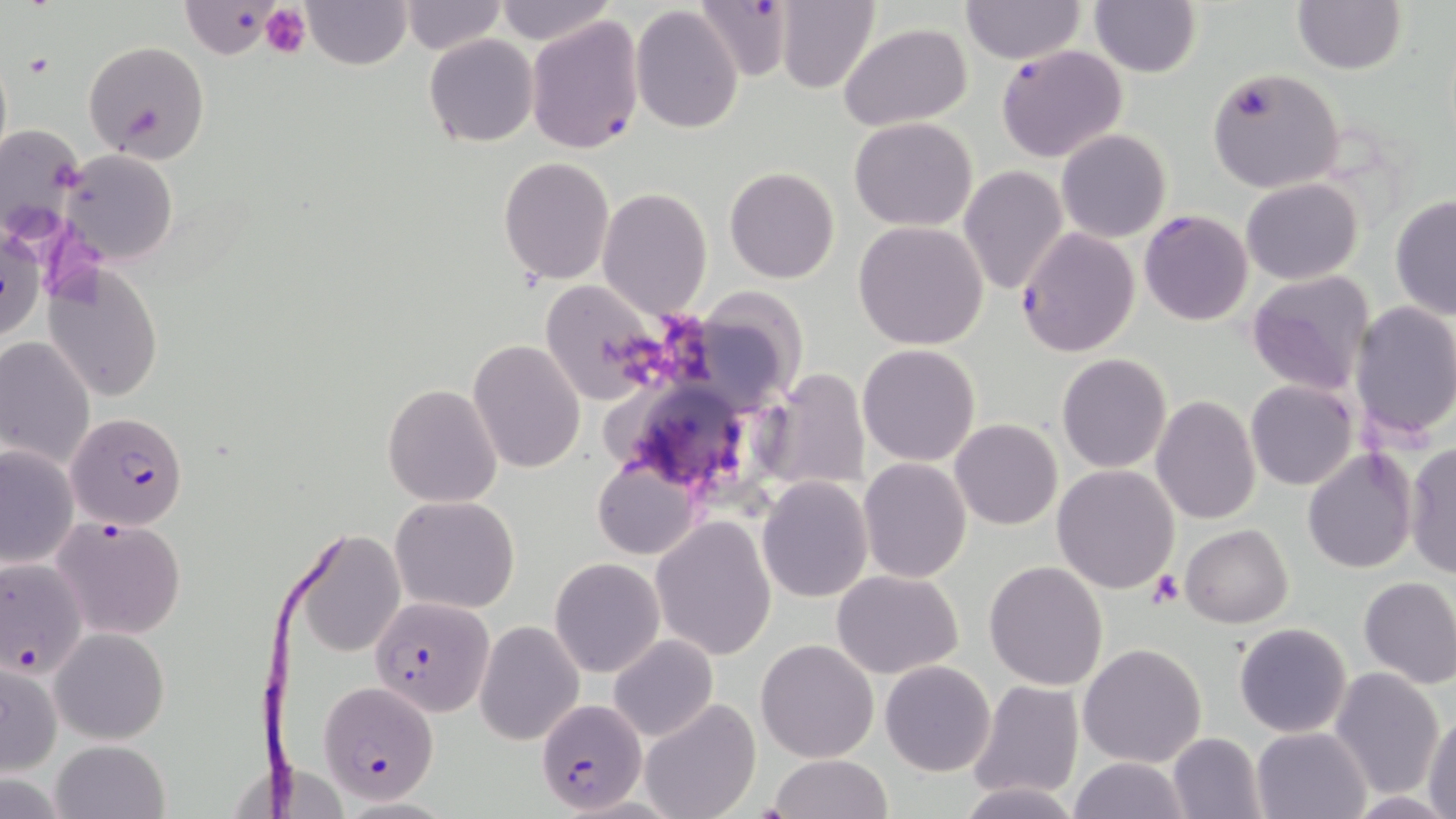
{
  "slide_level_diagnosis": "Plasmodium falciparum",
  "uninfected_red_blood_cell_locations": "approximate bounding boxes as (x1, y1, x2, y2) in pixels: (179, 0, 291, 60), (305, 0, 410, 70), (401, 0, 506, 55), (774, 0, 881, 94), (1088, 0, 1201, 77), (1292, 0, 1406, 74), (491, 1, 615, 47), (960, 1, 1087, 64), (631, 4, 743, 135), (838, 23, 970, 131), (424, 33, 537, 146), (83, 40, 210, 164), (1207, 68, 1346, 193), (848, 117, 977, 231), (1057, 130, 1171, 243), (58, 148, 179, 264), (499, 157, 614, 285), (958, 167, 1068, 295), (724, 168, 839, 283), (1242, 178, 1364, 285), (598, 187, 712, 320), (1389, 194, 1456, 320), (852, 222, 990, 351), (1, 225, 43, 346), (44, 265, 164, 403), (1247, 269, 1373, 397), (538, 281, 666, 404), (1349, 302, 1456, 441), (1, 336, 94, 472), (467, 340, 586, 475), (857, 343, 981, 466), (1057, 354, 1171, 473), (757, 367, 871, 495), (1246, 380, 1358, 490), (383, 383, 504, 507), (1151, 397, 1260, 522), (950, 419, 1062, 531), (1403, 442, 1456, 579), (1, 444, 78, 569), (1301, 445, 1418, 574), (858, 458, 972, 584), (593, 461, 698, 559), (1052, 465, 1180, 594), (756, 476, 873, 604), (391, 494, 520, 614), (650, 515, 778, 660), (1180, 523, 1293, 629), (291, 528, 406, 657), (550, 557, 664, 677), (984, 560, 1109, 690), (831, 569, 964, 677), (1357, 576, 1456, 689), (474, 620, 585, 747), (1234, 622, 1352, 738), (50, 627, 170, 745), (609, 634, 719, 742), (756, 639, 878, 762), (1078, 642, 1207, 768), (880, 660, 996, 776), (1, 661, 63, 777), (1330, 667, 1445, 796), (970, 681, 1085, 801), (640, 697, 760, 819), (1424, 710, 1456, 819), (1252, 727, 1372, 818), (1167, 732, 1266, 818), (50, 738, 171, 819), (768, 754, 895, 818), (1069, 756, 1190, 819), (954, 780, 1084, 819), (1348, 794, 1452, 818)",
  "field_of_view": "single",
  "modality": "optical microscopy",
  "image_size": "1456×819 pixels",
  "stain": "May-Grünwald-Giemsa",
  "platelet_locations": "approximate bounding boxes as (x1, y1, x2, y2) in pixels: (259, 4, 312, 60), (1149, 569, 1185, 608)",
  "preparation": "thin blood smear",
  "magnification": "1000x",
  "plasmodium_falciparum_infected_red_blood_cell_locations": "approximate bounding boxes as (x1, y1, x2, y2) in pixels: (690, 0, 797, 83), (525, 15, 645, 156), (996, 44, 1129, 165), (1139, 209, 1254, 326), (1016, 226, 1141, 358), (68, 410, 189, 532), (51, 515, 187, 641), (0, 554, 89, 682), (371, 593, 495, 716), (320, 681, 439, 803), (535, 696, 645, 815)"
}